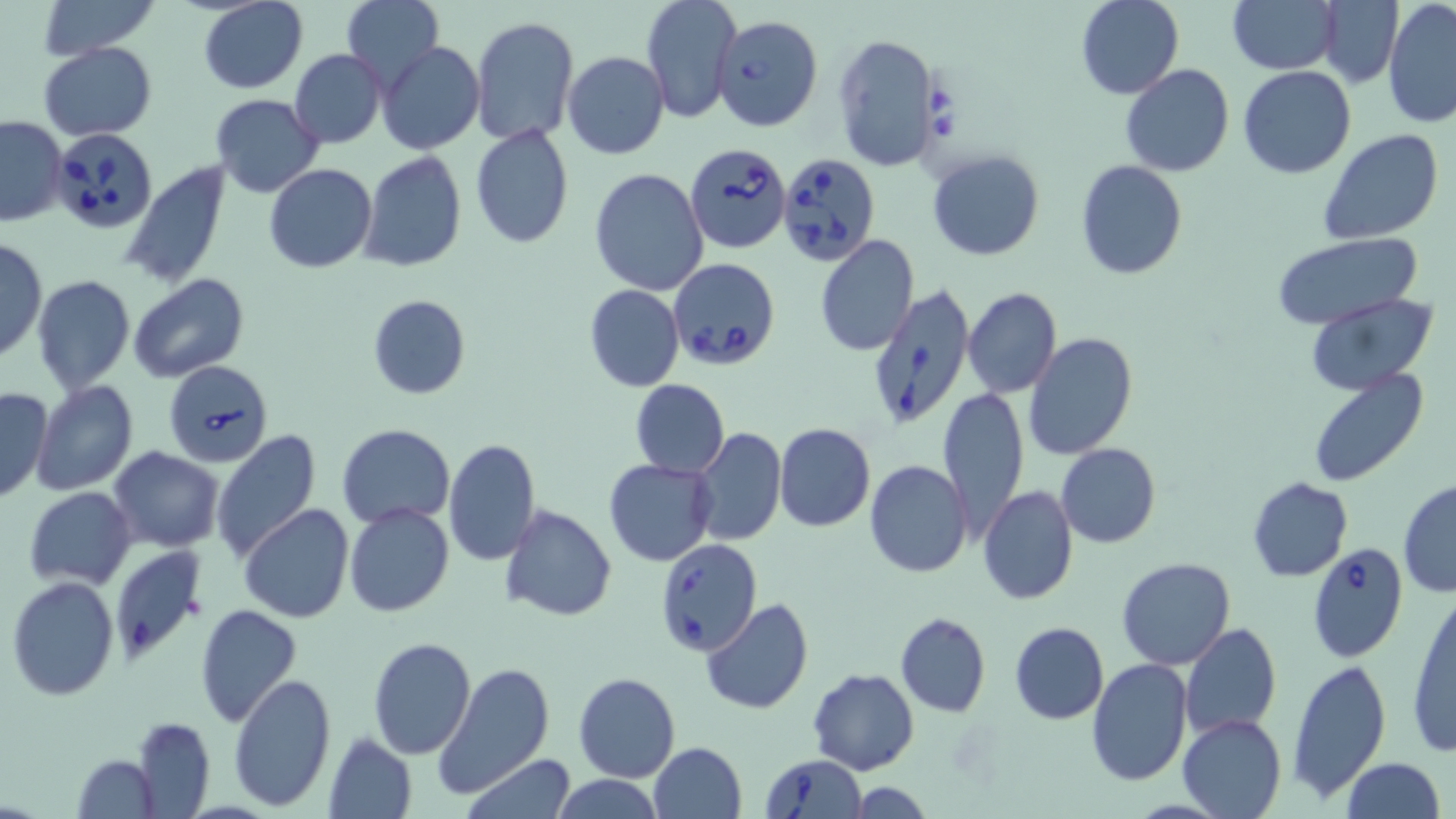

Summary:
  - Coordinate format: approximate bounding boxes as (x1, y1, x2, y2) in pixels
  - Babesia divergens-infected red blood cell locations: (712, 14, 823, 131), (52, 123, 155, 237), (685, 144, 792, 255), (776, 152, 882, 266), (667, 257, 779, 371), (866, 284, 978, 428), (164, 359, 272, 467), (656, 538, 763, 656), (108, 543, 209, 666), (1306, 543, 1408, 662), (761, 754, 865, 819)
  - Uninfected red blood cell locations: (33, 0, 163, 61), (198, 0, 307, 94), (641, 0, 741, 124), (1076, 0, 1184, 100), (1316, 0, 1404, 87), (341, 1, 444, 91), (1230, 1, 1337, 74), (1382, 1, 1456, 128), (470, 17, 579, 145), (832, 31, 941, 173), (371, 39, 476, 268), (39, 41, 157, 140), (378, 41, 485, 155), (288, 49, 386, 148), (562, 51, 669, 159), (1120, 65, 1235, 178), (1239, 67, 1356, 179), (210, 94, 324, 196), (0, 115, 68, 228), (470, 125, 573, 248), (1317, 129, 1442, 245), (925, 149, 1045, 261), (360, 152, 468, 272), (1076, 158, 1188, 279), (118, 160, 231, 291), (263, 163, 376, 273), (589, 168, 709, 296), (1269, 232, 1425, 329), (814, 236, 918, 355), (0, 237, 47, 364), (31, 274, 134, 393), (127, 274, 251, 384), (584, 284, 685, 392), (963, 288, 1061, 399), (1306, 293, 1436, 392), (366, 294, 472, 400), (1025, 333, 1138, 460), (1306, 370, 1429, 487), (629, 378, 729, 478), (31, 381, 138, 496), (0, 385, 52, 506), (939, 385, 1031, 544), (773, 422, 875, 532), (337, 423, 454, 527), (690, 428, 786, 547), (209, 430, 323, 563), (442, 437, 542, 566), (1055, 442, 1163, 548), (109, 446, 224, 553), (604, 457, 715, 567), (864, 460, 973, 580), (1246, 476, 1353, 583), (1397, 480, 1456, 597), (24, 486, 137, 588), (978, 486, 1078, 605), (344, 503, 455, 617), (240, 505, 353, 623), (499, 505, 617, 621), (1117, 557, 1236, 670), (7, 576, 119, 700), (1406, 590, 1456, 758), (700, 598, 814, 716), (194, 603, 303, 729), (895, 612, 989, 718), (1123, 621, 1247, 766), (1009, 622, 1108, 724), (1180, 622, 1281, 739), (368, 638, 476, 759), (1086, 659, 1192, 786), (1286, 659, 1390, 802), (434, 661, 554, 799), (809, 668, 919, 775), (573, 671, 681, 783), (228, 674, 336, 811), (1178, 712, 1286, 819), (133, 716, 215, 816), (322, 731, 417, 819), (647, 741, 747, 819), (70, 754, 161, 819), (460, 756, 578, 818), (1342, 758, 1445, 819), (552, 776, 665, 818), (848, 781, 936, 818)
  - Slide-level diagnosis: Babesia divergens
  - Magnification: 1000x
  - Preparation: thin blood smear
  - Modality: light microscopy
  - Stain: May-Grünwald-Giemsa
  - Field of view: single
  - Image size: 1456×819 pixels